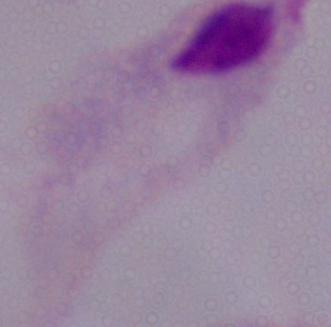

Summary:
  - Magnification: 1000x
  - Identification: trichomonad
  - Modality: micrograph